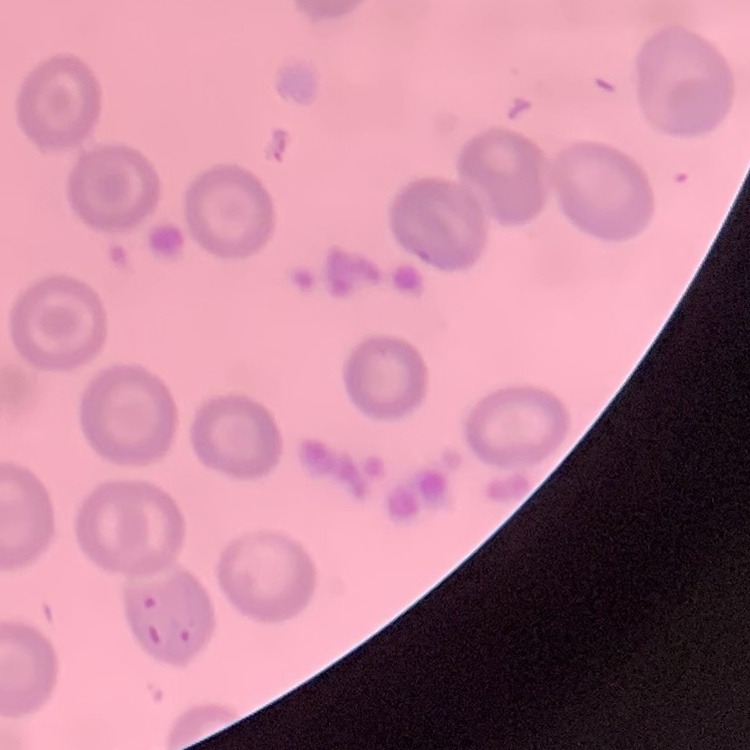

red blood cell morphology = no rouleaux formation
stain = Field's or Giemsa
image type = square crop of a larger photomicrograph
preparation = thin blood smear